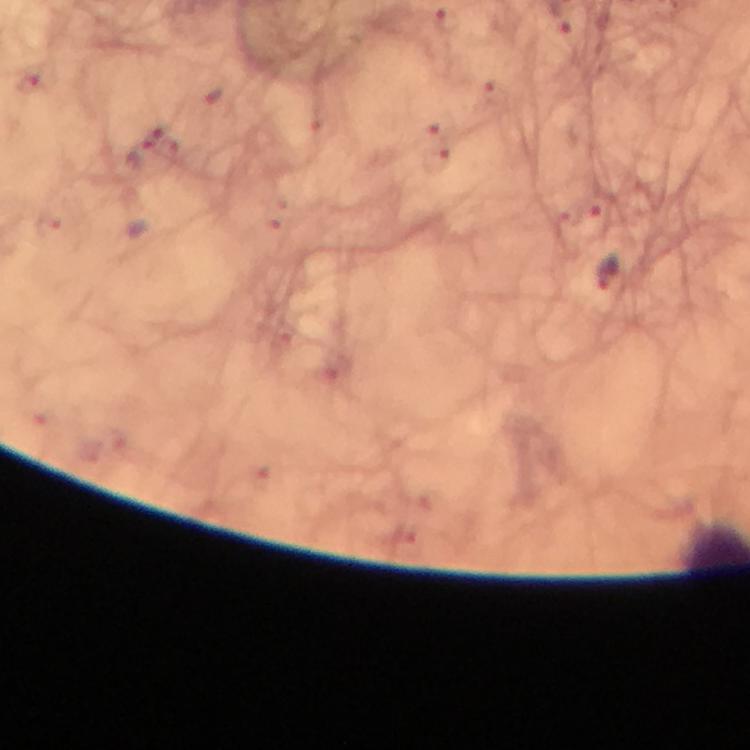

Approximate centers as {x, y} in pixels.
Summary:
  - Malaria parasite locations: {607, 274}
  - Cropped from: one field of view
  - Image size: 750×750 pixels
  - Preparation: thick blood smear
  - Capture: smartphone camera through the microscope
  - Stain: Giemsa
  - Context: from a malaria diagnostic workup
  - Magnification: 100x
  - Immersion oil: applied